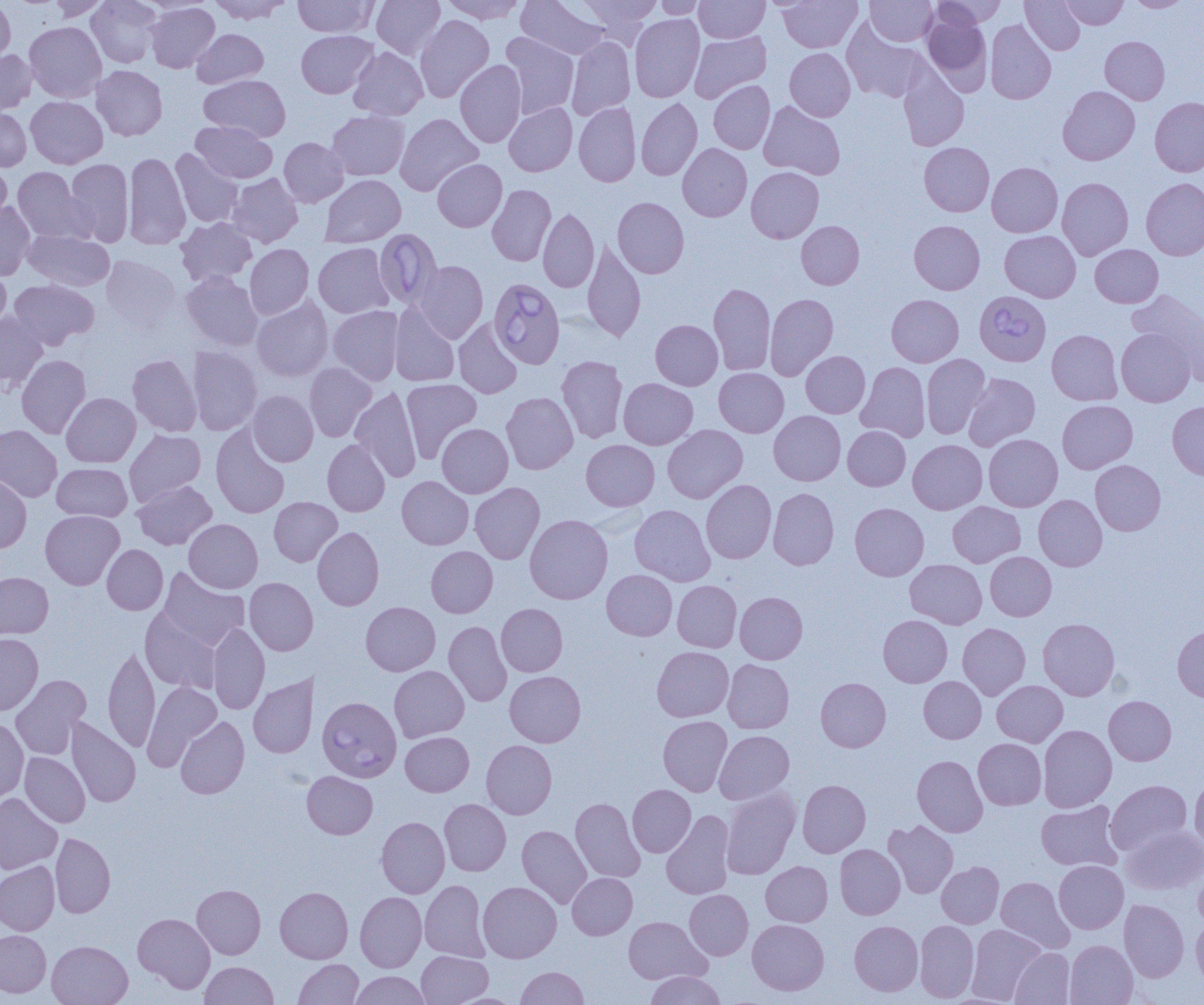
Summary:
  - Coordinate format: approximate bounding boxes as (x1,y1)-(x2,y2) corner pairs in pixels
  - Babesia divergens-infected red blood cell locations: (374,229)-(442,307), (489,277)-(565,368), (975,290)-(1051,366), (317,696)-(401,782)
  - Uninfected red blood cell locations: (0,0)-(16,67), (47,0)-(110,20), (87,0)-(163,67), (209,0)-(292,24), (293,0)-(378,37), (372,0)-(445,60), (440,0)-(526,24), (517,0)-(609,60), (576,0)-(660,43), (654,0)-(710,19), (694,0)-(769,43), (778,0)-(862,52), (866,0)-(937,46), (931,0)-(1007,29), (1020,0)-(1085,55), (1060,0)-(1127,29), (1126,0)-(1193,11), (146,2)-(220,72), (922,7)-(991,90), (630,14)-(705,102), (415,15)-(494,103), (985,19)-(1056,104), (24,21)-(106,102), (192,29)-(268,88), (296,30)-(378,98), (689,31)-(771,102), (500,32)-(579,119), (566,36)-(635,119), (1100,36)-(1169,104), (348,47)-(428,121), (0,48)-(36,115), (785,48)-(855,121), (455,60)-(527,147), (91,65)-(167,140), (899,66)-(969,151), (199,74)-(290,141), (709,81)-(774,154), (1058,86)-(1140,165), (26,96)-(107,168), (1150,97)-(1204,176), (636,98)-(702,180), (759,101)-(845,180), (574,102)-(641,187), (504,103)-(577,176), (0,106)-(31,172), (327,110)-(409,181), (395,113)-(483,196), (192,121)-(277,183), (279,137)-(348,207), (919,142)-(994,216), (678,143)-(752,221), (170,149)-(243,227), (123,151)-(191,250), (65,158)-(134,246), (433,159)-(507,232), (0,160)-(12,229), (986,162)-(1063,237), (746,166)-(824,243), (12,167)-(87,243), (227,173)-(303,247), (320,174)-(406,247), (1057,177)-(1133,260), (1141,178)-(1204,260), (487,184)-(555,266), (612,197)-(689,278), (0,201)-(35,280), (538,208)-(599,292), (176,218)-(257,287), (909,220)-(985,295), (796,221)-(864,289), (23,229)-(114,291), (1000,230)-(1081,302), (582,240)-(646,341), (313,243)-(393,318), (245,244)-(314,319), (1091,244)-(1163,308), (101,255)-(181,330), (414,260)-(488,343), (0,264)-(11,335), (181,271)-(263,351), (9,279)-(100,350), (708,283)-(775,375), (1127,289)-(1203,372), (765,293)-(838,380), (886,294)-(963,367), (251,296)-(333,382), (390,303)-(460,387), (328,305)-(404,385), (0,312)-(48,391), (453,318)-(522,399), (651,320)-(723,390), (1116,328)-(1195,406), (1046,330)-(1122,405), (187,346)-(263,435), (801,351)-(870,418), (17,354)-(91,438), (128,354)-(201,436), (921,354)-(990,438), (557,356)-(628,443), (304,362)-(376,442), (856,362)-(930,442), (714,368)-(788,437), (963,373)-(1040,450), (619,378)-(697,449), (401,379)-(482,462), (350,386)-(422,483), (248,390)-(318,466), (501,392)-(578,474), (61,393)-(141,467), (1057,400)-(1138,473), (1167,401)-(1204,480), (769,410)-(845,485), (437,423)-(513,497), (211,424)-(289,518), (0,425)-(62,502), (662,425)-(747,503), (843,426)-(910,490), (124,429)-(206,506), (984,434)-(1063,511), (322,439)-(390,516), (908,439)-(987,514), (581,440)-(659,510), (1090,460)-(1165,535), (52,463)-(132,521), (0,475)-(31,553), (397,476)-(473,549), (701,479)-(776,563), (132,480)-(217,550), (469,482)-(544,564), (768,488)-(839,570), (1033,494)-(1107,571), (269,497)-(342,566), (947,501)-(1025,567), (850,503)-(929,580), (630,504)-(714,585), (41,510)-(124,589), (525,514)-(612,604), (184,519)-(263,593), (312,527)-(384,610), (102,544)-(168,614), (426,546)-(497,617), (985,551)-(1056,621), (906,559)-(987,628), (158,568)-(250,650), (602,570)-(677,640), (0,572)-(53,640), (244,577)-(318,655), (672,581)-(741,652), (735,592)-(807,664), (361,601)-(440,675), (496,603)-(567,676), (140,608)-(220,693), (878,615)-(952,687), (1038,618)-(1120,700), (444,621)-(512,707), (208,622)-(269,714), (958,623)-(1030,700), (1172,624)-(1204,703), (0,633)-(43,715), (103,644)-(160,752), (652,646)-(734,722), (723,659)-(794,733), (389,666)-(469,742), (505,671)-(585,747), (248,674)-(318,758), (11,675)-(91,760), (919,676)-(986,743), (815,677)-(891,752), (992,680)-(1067,747), (142,681)-(221,771), (1104,695)-(1176,765), (0,716)-(29,802), (658,716)-(732,796), (65,717)-(140,807), (175,717)-(249,798), (1038,725)-(1116,812), (714,730)-(794,804), (401,732)-(473,796), (973,738)-(1046,810), (482,740)-(557,819), (20,752)-(90,827), (912,755)-(987,837), (302,771)-(377,838), (1189,774)-(1204,853), (797,780)-(870,857), (1105,780)-(1192,854), (627,784)-(696,857), (721,786)-(800,880), (0,793)-(63,874), (571,798)-(645,882), (439,799)-(511,876), (1036,800)-(1123,871), (662,811)-(735,899), (376,816)-(450,898), (883,820)-(958,898), (517,825)-(592,908), (1122,825)-(1204,896), (50,833)-(115,917), (835,844)-(905,919), (1054,860)-(1128,934), (0,861)-(59,935), (761,861)-(832,926), (936,861)-(1004,928), (1193,863)-(1204,930), (568,873)-(637,939), (996,876)-(1075,954), (420,880)-(490,962), (478,881)-(561,962), (192,884)-(265,959), (275,887)-(353,963), (684,889)-(753,960), (355,891)-(426,972), (1119,899)-(1188,982), (133,913)-(215,992), (1191,915)-(1204,988), (623,916)-(710,984), (747,919)-(829,995), (850,920)-(923,996), (914,920)-(979,1003), (967,924)-(1046,1004), (0,930)-(51,997), (47,940)-(132,1005), (1065,940)-(1137,1005), (1009,947)-(1075,1004), (416,950)-(493,1005), (294,959)-(363,1005), (200,961)-(278,1004), (516,966)-(588,1005), (350,971)-(430,1005), (645,971)-(727,1005)
  - Slide-level diagnosis: Babesia divergens
  - Modality: light microscopy
  - Preparation: thin blood film
  - Image size: 1204×1005 pixels
  - Field of view: single
  - Magnification: 1000x